Report the malaria status of this cell.
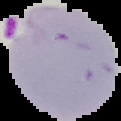
It is parasitized.

Cell region segmented out of the field of view; the surrounding area is masked to black. Image is 121×121 pixels. From a thin blood smear.